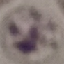
Result: no malaria parasites seen. Acquired by smartphone through the microscope eyepiece. Cell patch, automatically extracted from a larger field of view and resized to 64 × 64 pixels. Giemsa stain. Thin blood smear.